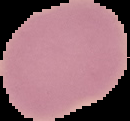

Summary:
  - Malaria status: uninfected
  - Preparation: thin blood film
  - Image size: 130×121 pixels
  - Image type: segmented cell region on a black background